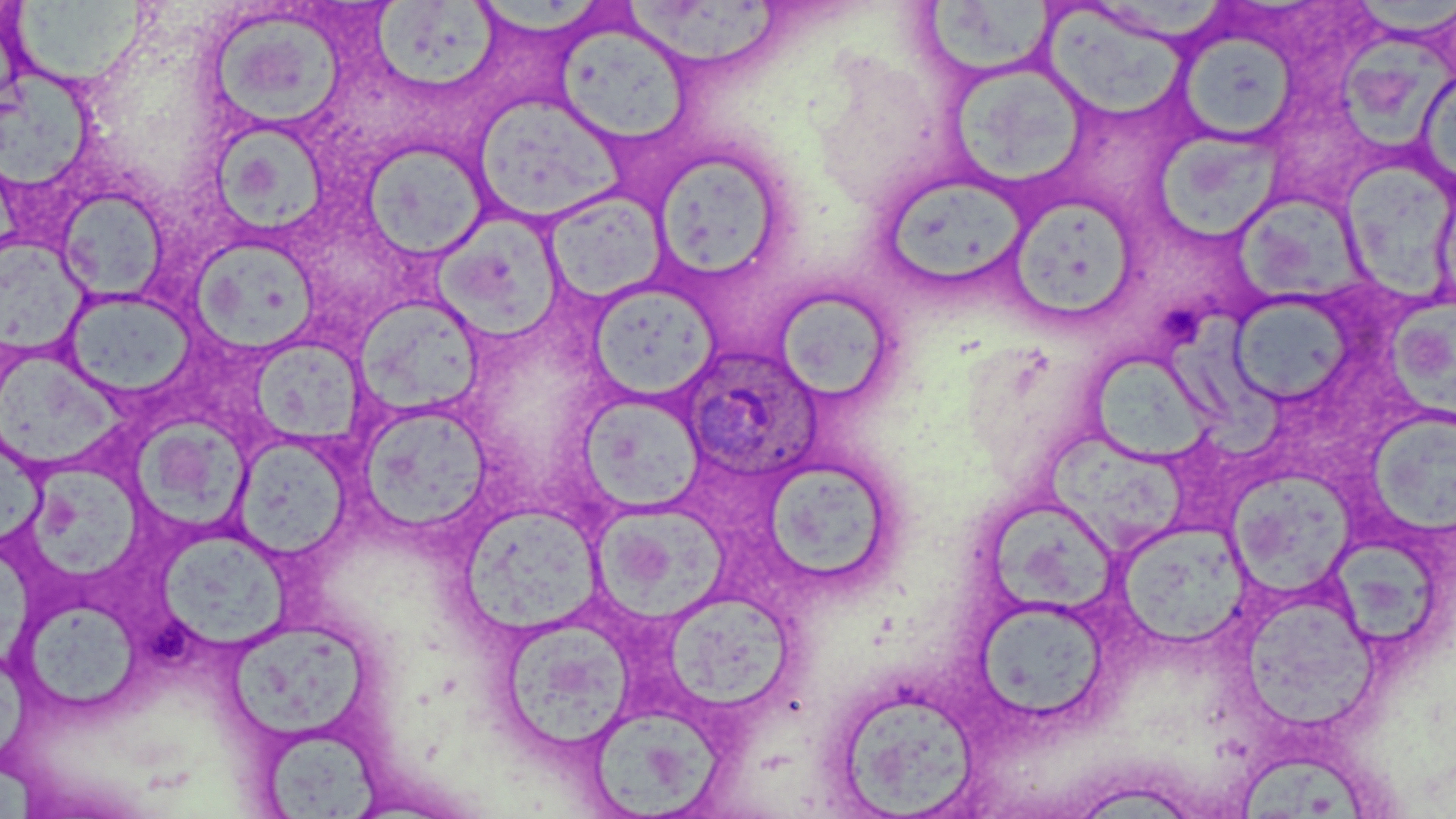

Approximate bounding boxes as named x1/y1/x2/y2 corners in pixels. Platelet locations: (x1=1161, y1=301, x2=1208, y2=348), (x1=145, y1=616, x2=196, y2=663). Plasmodium ovale-infected red blood cell locations: (x1=676, y1=344, x2=823, y2=482). Uninfected red blood cell locations: (x1=8, y1=0, x2=149, y2=86), (x1=485, y1=0, x2=603, y2=38), (x1=626, y1=2, x2=783, y2=70), (x1=374, y1=3, x2=505, y2=89), (x1=929, y1=3, x2=1059, y2=74), (x1=1354, y1=3, x2=1456, y2=39), (x1=1042, y1=5, x2=1203, y2=121), (x1=208, y1=13, x2=347, y2=128), (x1=557, y1=21, x2=692, y2=144), (x1=1177, y1=31, x2=1298, y2=142), (x1=1335, y1=37, x2=1453, y2=148), (x1=946, y1=60, x2=1089, y2=188), (x1=1416, y1=67, x2=1456, y2=200), (x1=1, y1=70, x2=95, y2=194), (x1=477, y1=102, x2=633, y2=233), (x1=206, y1=131, x2=334, y2=234), (x1=1157, y1=132, x2=1295, y2=249), (x1=361, y1=141, x2=490, y2=261), (x1=648, y1=148, x2=790, y2=284), (x1=1338, y1=153, x2=1456, y2=300), (x1=878, y1=172, x2=1032, y2=293), (x1=56, y1=186, x2=170, y2=303), (x1=542, y1=190, x2=670, y2=304), (x1=1006, y1=196, x2=1142, y2=325), (x1=1231, y1=196, x2=1375, y2=308), (x1=432, y1=218, x2=567, y2=347), (x1=0, y1=244, x2=96, y2=356), (x1=186, y1=246, x2=323, y2=356), (x1=588, y1=282, x2=718, y2=400), (x1=770, y1=286, x2=898, y2=405), (x1=61, y1=288, x2=199, y2=403), (x1=1227, y1=292, x2=1359, y2=408), (x1=1390, y1=296, x2=1456, y2=420), (x1=353, y1=297, x2=487, y2=419), (x1=1173, y1=309, x2=1288, y2=460), (x1=255, y1=338, x2=367, y2=447), (x1=1083, y1=353, x2=1217, y2=459), (x1=0, y1=358, x2=137, y2=471), (x1=357, y1=402, x2=494, y2=537), (x1=583, y1=403, x2=708, y2=517), (x1=1369, y1=408, x2=1456, y2=537), (x1=130, y1=423, x2=253, y2=528), (x1=1042, y1=432, x2=1193, y2=556), (x1=236, y1=442, x2=355, y2=566), (x1=0, y1=451, x2=55, y2=550), (x1=759, y1=456, x2=898, y2=589), (x1=1227, y1=470, x2=1358, y2=597), (x1=35, y1=471, x2=146, y2=578), (x1=984, y1=501, x2=1121, y2=617), (x1=594, y1=511, x2=737, y2=621), (x1=461, y1=513, x2=607, y2=635), (x1=1119, y1=523, x2=1249, y2=651), (x1=158, y1=537, x2=298, y2=650), (x1=1333, y1=541, x2=1441, y2=650), (x1=669, y1=594, x2=795, y2=710), (x1=31, y1=605, x2=147, y2=707), (x1=1245, y1=606, x2=1385, y2=733), (x1=977, y1=609, x2=1113, y2=722), (x1=498, y1=617, x2=636, y2=756), (x1=233, y1=627, x2=371, y2=735), (x1=829, y1=683, x2=983, y2=817), (x1=586, y1=705, x2=723, y2=815), (x1=263, y1=734, x2=379, y2=819), (x1=1232, y1=755, x2=1373, y2=819). Slide-level diagnosis: Plasmodium ovale. Optical microscopy. Thin blood smear. Image is 1456×819 pixels. May-Grünwald-Giemsa stain. Captured at 1000x magnification. One field of a larger specimen.